Outline each Babesia divergens-infected red blood cell.
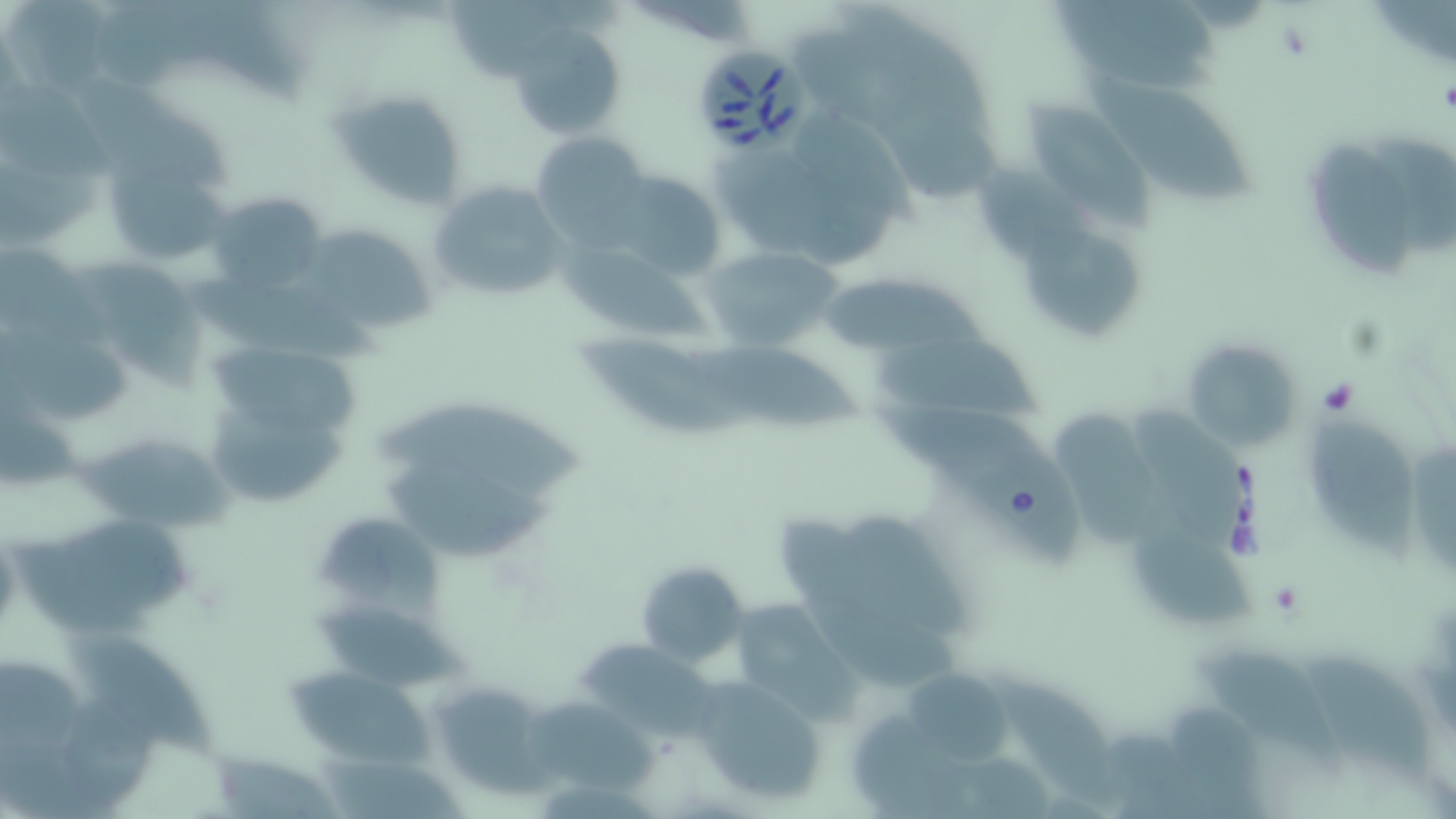

Approximate bounding boxes as (x1, y1, x2, y2) in pixels.
Babesia divergens-infected red blood cells: (697, 49, 819, 158).

Summary:
  - Platelet locations: (1438, 79, 1456, 117)
  - Uninfected red blood cell locations: (448, 2, 578, 84), (507, 25, 628, 142), (1090, 75, 1256, 200), (16, 76, 119, 178), (330, 88, 467, 210), (1031, 102, 1158, 222), (1365, 123, 1456, 265), (530, 129, 659, 244), (1311, 141, 1417, 288), (705, 151, 890, 269), (107, 157, 230, 270), (976, 162, 1105, 275), (609, 166, 729, 275), (428, 179, 567, 304), (207, 193, 330, 293), (291, 214, 441, 330), (1026, 218, 1141, 343), (551, 233, 715, 342), (701, 245, 849, 354), (78, 259, 208, 386), (192, 264, 389, 369), (824, 275, 1007, 358), (19, 311, 137, 420), (873, 330, 1052, 424), (576, 331, 745, 436), (1181, 338, 1306, 452), (692, 339, 862, 428), (210, 342, 358, 437), (370, 386, 589, 507), (1141, 403, 1248, 551), (875, 405, 1081, 576), (206, 407, 357, 507), (1048, 411, 1176, 555), (1308, 421, 1425, 570), (78, 425, 240, 536), (1408, 437, 1456, 580), (369, 458, 562, 563), (311, 511, 452, 622), (1134, 512, 1260, 629), (52, 513, 194, 613), (772, 515, 953, 685), (635, 559, 750, 668), (724, 597, 857, 715), (311, 603, 476, 697), (60, 625, 235, 764), (582, 639, 732, 749), (1200, 646, 1346, 768), (1303, 661, 1440, 784), (286, 667, 429, 769), (905, 673, 1022, 765), (996, 673, 1129, 814), (688, 675, 828, 805), (428, 681, 552, 800), (519, 694, 666, 791), (206, 741, 350, 819)
  - Slide-level diagnosis: Babesia divergens
  - Preparation: thin blood film
  - Stain: May-Grünwald-Giemsa
  - Image size: 1456×819 pixels
  - Modality: optical microscopy
  - Field of view: single
  - Magnification: 1000x